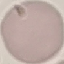

result: negative for malaria parasites
preparation: thin blood film
capture: smartphone through the microscope eyepiece
stain: Giemsa
image_type: cell patch, automatically extracted from a larger field of view and resized to 64 × 64 pixels